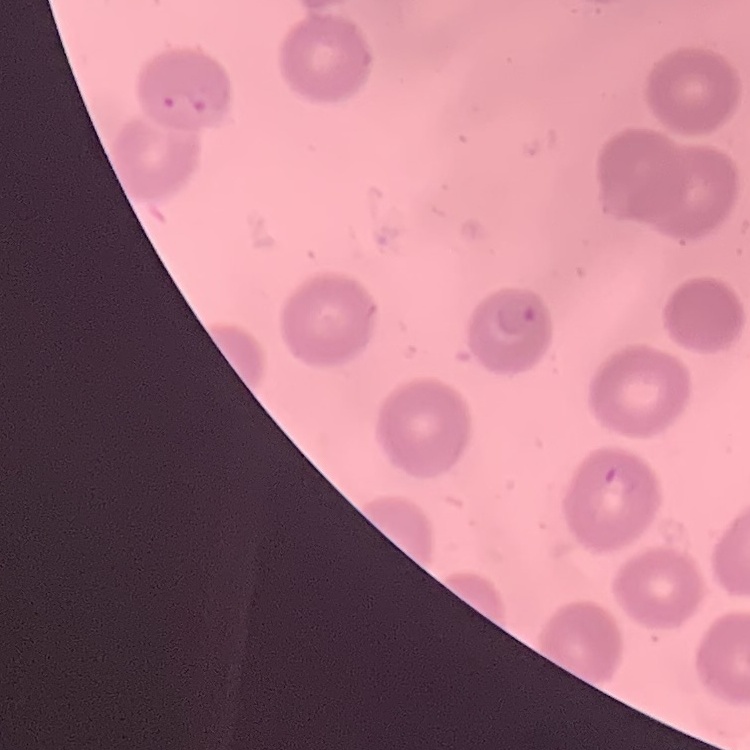

erythrocyte morphology = no rouleaux formation
image type = square crop of a larger photomicrograph
preparation = thin blood film
stain = Field's or Giemsa